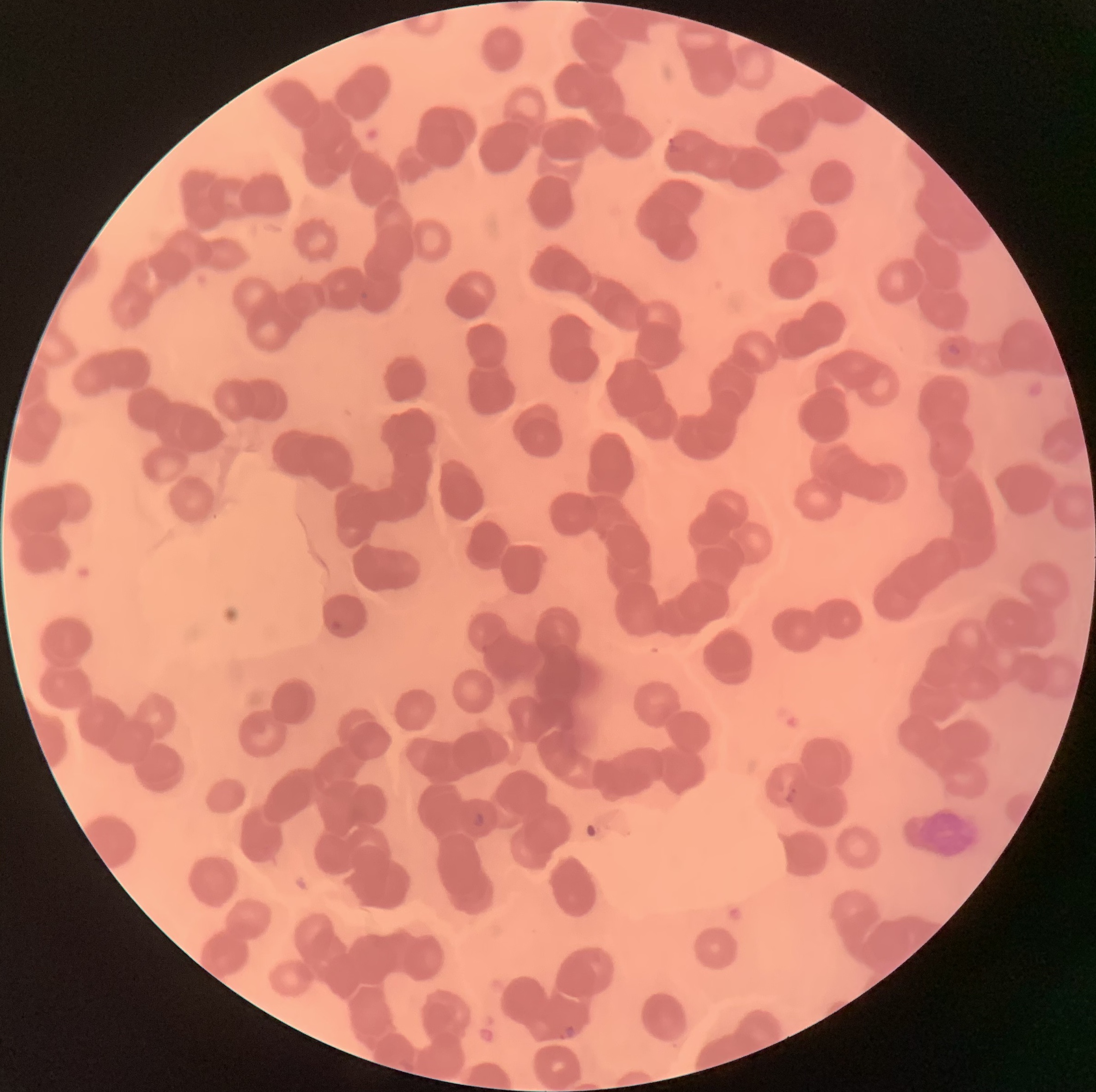
coordinate format = approximate bounding boxes as (x1,y1)-(x2,y2) corner pairs in pixels
Plasmodium parasite locations = (668,137)-(685,154), (360,291)-(370,301), (946,342)-(964,357), (329,621)-(341,634), (786,787)-(798,802), (473,812)-(486,828), (559,1024)-(575,1040)
modality = optical microscopy
red blood cell morphology = rouleaux formation
image size = 1096×1092 pixels
preparation = thin blood film